Name the blood parasite species.
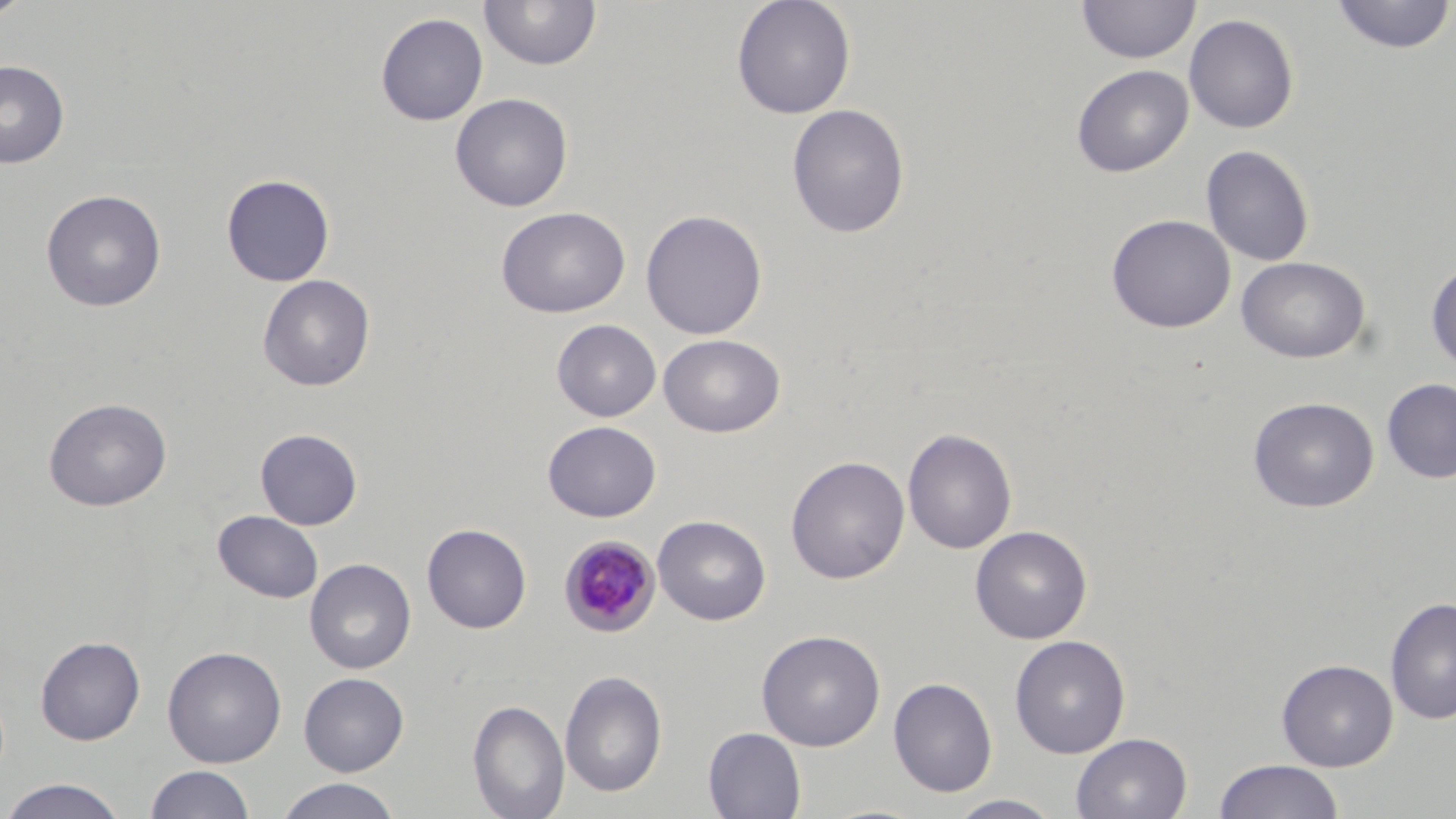
Plasmodium malariae.

Approximate bounding boxes as [x1, y1, x2, y2] in pixels. Uninfected red blood cell locations: [0, 0, 32, 22], [731, 0, 856, 119], [1077, 0, 1200, 64], [1330, 0, 1455, 55], [478, 1, 602, 72], [375, 12, 488, 125], [1184, 13, 1300, 134], [0, 60, 69, 168], [1071, 64, 1194, 178], [450, 92, 573, 212], [787, 103, 910, 238], [1201, 145, 1314, 267], [221, 173, 335, 287], [40, 188, 167, 312], [495, 206, 631, 318], [641, 209, 767, 340], [1106, 213, 1236, 333], [1236, 256, 1371, 363], [1426, 260, 1456, 372], [257, 274, 375, 391], [551, 319, 661, 422], [658, 334, 785, 437], [1381, 379, 1456, 483], [1248, 396, 1379, 512], [43, 397, 171, 511], [542, 420, 661, 522], [255, 428, 363, 530], [903, 428, 1017, 554], [786, 455, 910, 584], [213, 510, 324, 603], [652, 514, 771, 625], [422, 523, 532, 633], [970, 526, 1092, 644], [305, 558, 416, 674], [1385, 596, 1456, 724], [756, 629, 886, 751], [1009, 634, 1131, 758], [35, 635, 145, 745], [162, 645, 287, 767], [1277, 659, 1398, 771], [559, 669, 668, 797], [298, 672, 409, 776], [888, 677, 997, 797], [468, 699, 570, 819], [703, 727, 806, 818], [1071, 733, 1192, 819], [1213, 760, 1345, 819], [144, 765, 256, 818], [1, 778, 131, 818], [274, 778, 402, 818], [947, 794, 1064, 819]. Plasmodium malariae-infected red blood cell locations: [559, 535, 662, 636]. Image is 1456×819 pixels. Thin blood smear. One field of a larger specimen. Captured at 1000x magnification. May-Grünwald-Giemsa-stained preparation. Light microscopy.